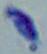
{
  "identification": "Toxoplasma gondii",
  "magnification": "1000x",
  "modality": "photomicrograph"
}